Classify this cell by malaria status.
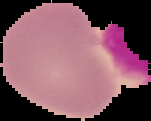

It is uninfected.

Summary:
  - Image size: 151×121 pixels
  - Image type: segmented cell region on a black background
  - Preparation: thin blood film